Report the malaria status of this cell.
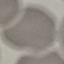
It is uninfected.

Summary:
  - Preparation: thin smear
  - Capture: smartphone camera at the microscope eyepiece
  - Stain: Giemsa
  - Image type: automatically extracted cell patch, resized to 64 × 64 pixels